Name the blood parasite species.
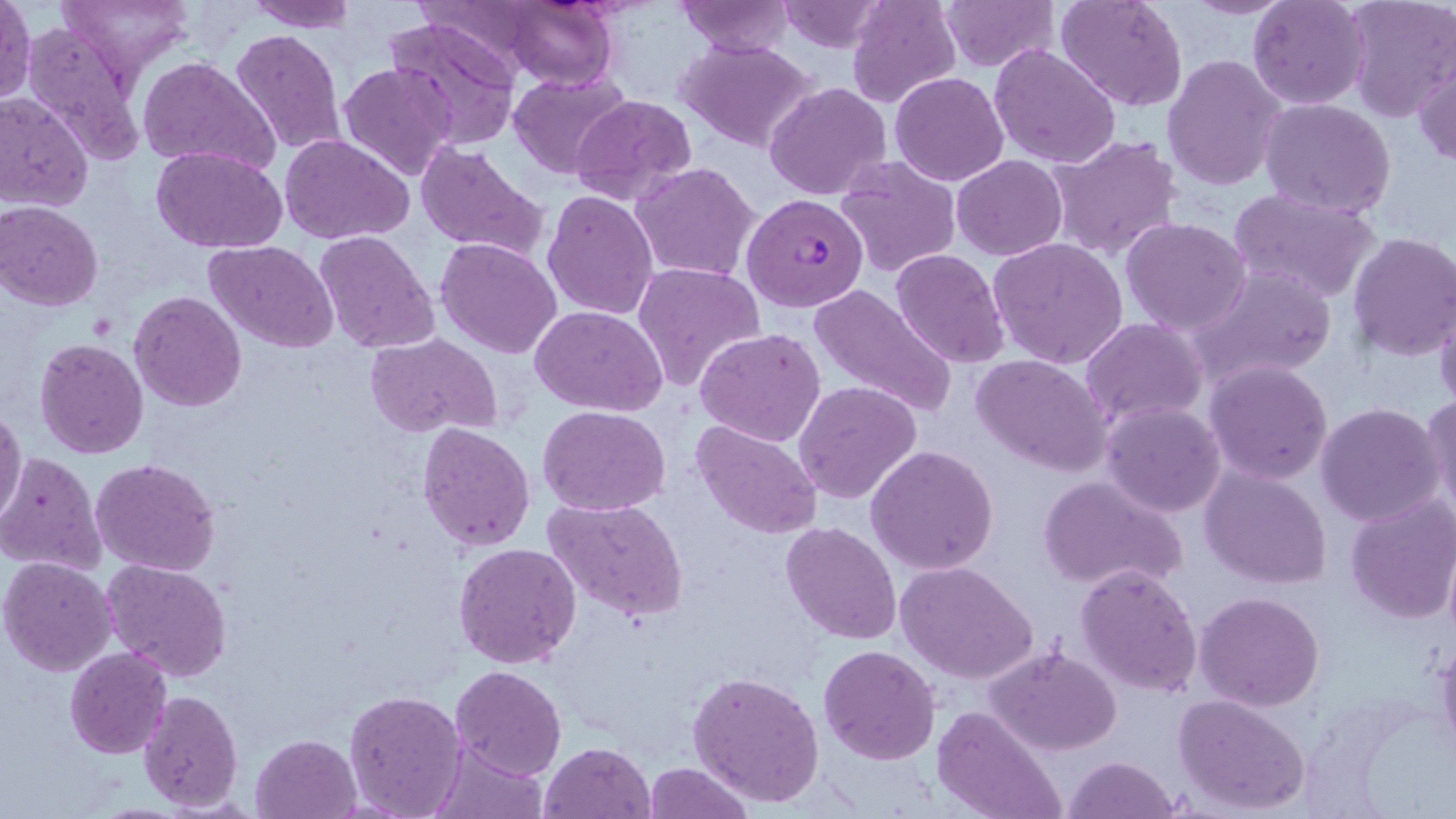
Plasmodium falciparum.

Summary:
  - Coordinate format: approximate bounding boxes as named x1/y1/x2/y2 corners in pixels
  - Plasmodium falciparum-infected red blood cell locations: (x1=742, y1=192, x2=868, y2=311)
  - Uninfected red blood cell locations: (x1=0, y1=0, x2=35, y2=106), (x1=59, y1=0, x2=195, y2=78), (x1=242, y1=0, x2=358, y2=32), (x1=778, y1=0, x2=888, y2=52), (x1=847, y1=0, x2=961, y2=108), (x1=937, y1=0, x2=1056, y2=71), (x1=1054, y1=0, x2=1188, y2=112), (x1=1182, y1=0, x2=1296, y2=18), (x1=1249, y1=0, x2=1371, y2=109), (x1=1343, y1=0, x2=1454, y2=119), (x1=674, y1=1, x2=797, y2=57), (x1=496, y1=3, x2=625, y2=89), (x1=382, y1=14, x2=519, y2=148), (x1=21, y1=17, x2=146, y2=167), (x1=229, y1=28, x2=346, y2=158), (x1=677, y1=38, x2=821, y2=153), (x1=989, y1=43, x2=1122, y2=169), (x1=1413, y1=54, x2=1456, y2=166), (x1=1163, y1=55, x2=1286, y2=191), (x1=137, y1=56, x2=280, y2=176), (x1=337, y1=62, x2=459, y2=183), (x1=509, y1=72, x2=631, y2=179), (x1=889, y1=73, x2=1009, y2=187), (x1=765, y1=82, x2=893, y2=201), (x1=0, y1=92, x2=94, y2=210), (x1=569, y1=94, x2=695, y2=207), (x1=1260, y1=98, x2=1396, y2=218), (x1=279, y1=134, x2=414, y2=245), (x1=1046, y1=134, x2=1183, y2=261), (x1=414, y1=141, x2=550, y2=263), (x1=151, y1=146, x2=289, y2=253), (x1=836, y1=155, x2=961, y2=277), (x1=953, y1=155, x2=1067, y2=260), (x1=631, y1=161, x2=761, y2=282), (x1=543, y1=189, x2=659, y2=321), (x1=1229, y1=189, x2=1380, y2=304), (x1=1, y1=202, x2=103, y2=310), (x1=1122, y1=217, x2=1252, y2=335), (x1=312, y1=231, x2=438, y2=353), (x1=1347, y1=231, x2=1456, y2=359), (x1=435, y1=236, x2=563, y2=358), (x1=989, y1=237, x2=1128, y2=369), (x1=204, y1=240, x2=340, y2=353), (x1=891, y1=249, x2=1012, y2=368), (x1=632, y1=261, x2=765, y2=392), (x1=1192, y1=264, x2=1336, y2=385), (x1=809, y1=282, x2=956, y2=419), (x1=1433, y1=287, x2=1456, y2=414), (x1=130, y1=291, x2=246, y2=410), (x1=531, y1=305, x2=667, y2=417), (x1=1081, y1=318, x2=1208, y2=426), (x1=694, y1=328, x2=826, y2=448), (x1=365, y1=333, x2=501, y2=439), (x1=35, y1=338, x2=150, y2=459), (x1=972, y1=354, x2=1113, y2=476), (x1=1204, y1=360, x2=1334, y2=486), (x1=794, y1=379, x2=922, y2=504), (x1=1420, y1=393, x2=1456, y2=524), (x1=1099, y1=401, x2=1226, y2=517), (x1=1315, y1=403, x2=1447, y2=527), (x1=538, y1=405, x2=671, y2=514), (x1=0, y1=407, x2=26, y2=523), (x1=691, y1=420, x2=822, y2=538), (x1=417, y1=422, x2=536, y2=551), (x1=867, y1=444, x2=999, y2=575), (x1=1, y1=452, x2=105, y2=575), (x1=90, y1=456, x2=221, y2=575), (x1=1200, y1=466, x2=1332, y2=588), (x1=1038, y1=475, x2=1188, y2=595), (x1=1345, y1=495, x2=1456, y2=624), (x1=543, y1=496, x2=689, y2=625), (x1=781, y1=520, x2=903, y2=645), (x1=1442, y1=538, x2=1456, y2=643), (x1=453, y1=541, x2=581, y2=668), (x1=1, y1=557, x2=118, y2=676), (x1=103, y1=558, x2=233, y2=681), (x1=898, y1=562, x2=1038, y2=684), (x1=1075, y1=563, x2=1202, y2=699), (x1=1195, y1=590, x2=1325, y2=711), (x1=1434, y1=637, x2=1456, y2=763), (x1=818, y1=645, x2=940, y2=765), (x1=987, y1=645, x2=1122, y2=756), (x1=64, y1=648, x2=174, y2=760), (x1=450, y1=665, x2=567, y2=780), (x1=688, y1=669, x2=826, y2=808), (x1=343, y1=687, x2=467, y2=819), (x1=136, y1=689, x2=243, y2=810), (x1=1173, y1=693, x2=1313, y2=816), (x1=933, y1=705, x2=1066, y2=819), (x1=250, y1=733, x2=362, y2=819), (x1=427, y1=739, x2=548, y2=817), (x1=538, y1=741, x2=655, y2=819), (x1=1063, y1=754, x2=1182, y2=819), (x1=644, y1=761, x2=752, y2=817)
  - Field of view: one of a larger specimen
  - Image size: 1456×819 pixels
  - Magnification: 1000x
  - Preparation: thin blood smear
  - Modality: light microscopy
  - Stain: May-Grünwald-Giemsa